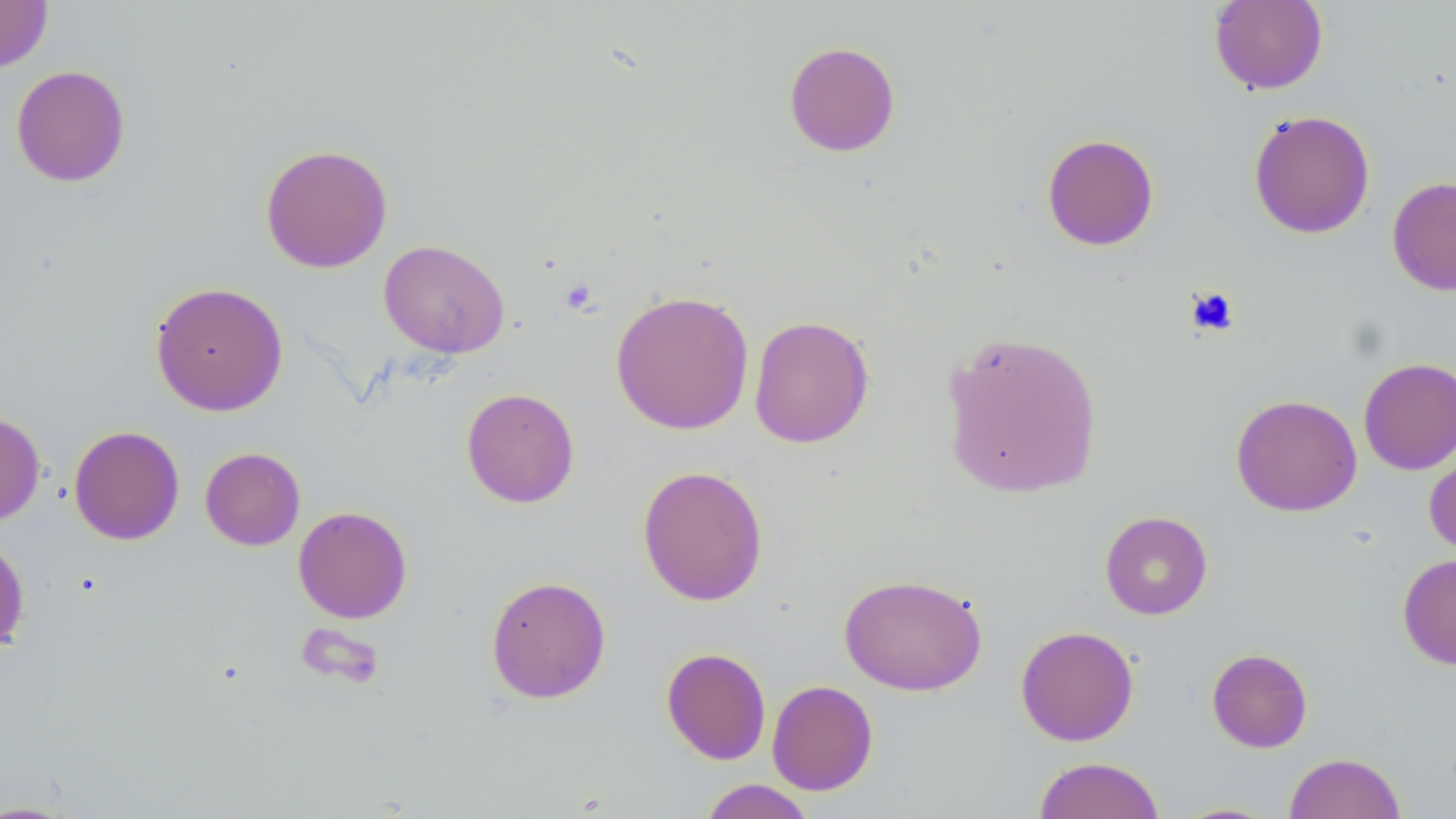

Summary:
  - Coordinate format: approximate bounding boxes as (x1, y1, x2, y2) in pixels
  - Uninfected red blood cell locations: (0, 0, 53, 72), (1209, 0, 1328, 95), (783, 40, 901, 157), (10, 64, 130, 188), (1248, 109, 1375, 239), (1041, 133, 1159, 251), (260, 143, 393, 273), (1387, 175, 1456, 296), (379, 239, 509, 358), (149, 281, 288, 416), (610, 290, 755, 435), (749, 315, 874, 448), (939, 329, 1104, 499), (1358, 357, 1456, 475), (461, 387, 580, 507), (1230, 394, 1362, 517), (0, 410, 45, 526), (68, 425, 185, 545), (1424, 439, 1456, 559), (200, 447, 305, 550), (637, 465, 768, 606), (293, 505, 413, 624), (1100, 511, 1213, 619), (0, 535, 30, 655), (1397, 553, 1456, 670), (839, 573, 988, 696), (485, 574, 612, 704), (1015, 625, 1139, 746), (661, 647, 771, 764), (1206, 647, 1313, 753), (766, 679, 878, 796), (1284, 752, 1406, 819), (1033, 756, 1165, 819), (696, 779, 818, 818), (0, 799, 84, 818), (1169, 801, 1282, 818)
  - Platelet locations: (559, 277, 600, 316), (1185, 285, 1239, 338)
  - Slide-level diagnosis: negative for blood parasites
  - Magnification: 1000x
  - Preparation: thin blood smear
  - Stain: May-Grünwald-Giemsa
  - Modality: light microscopy
  - Image size: 1456×819 pixels
  - Field of view: single